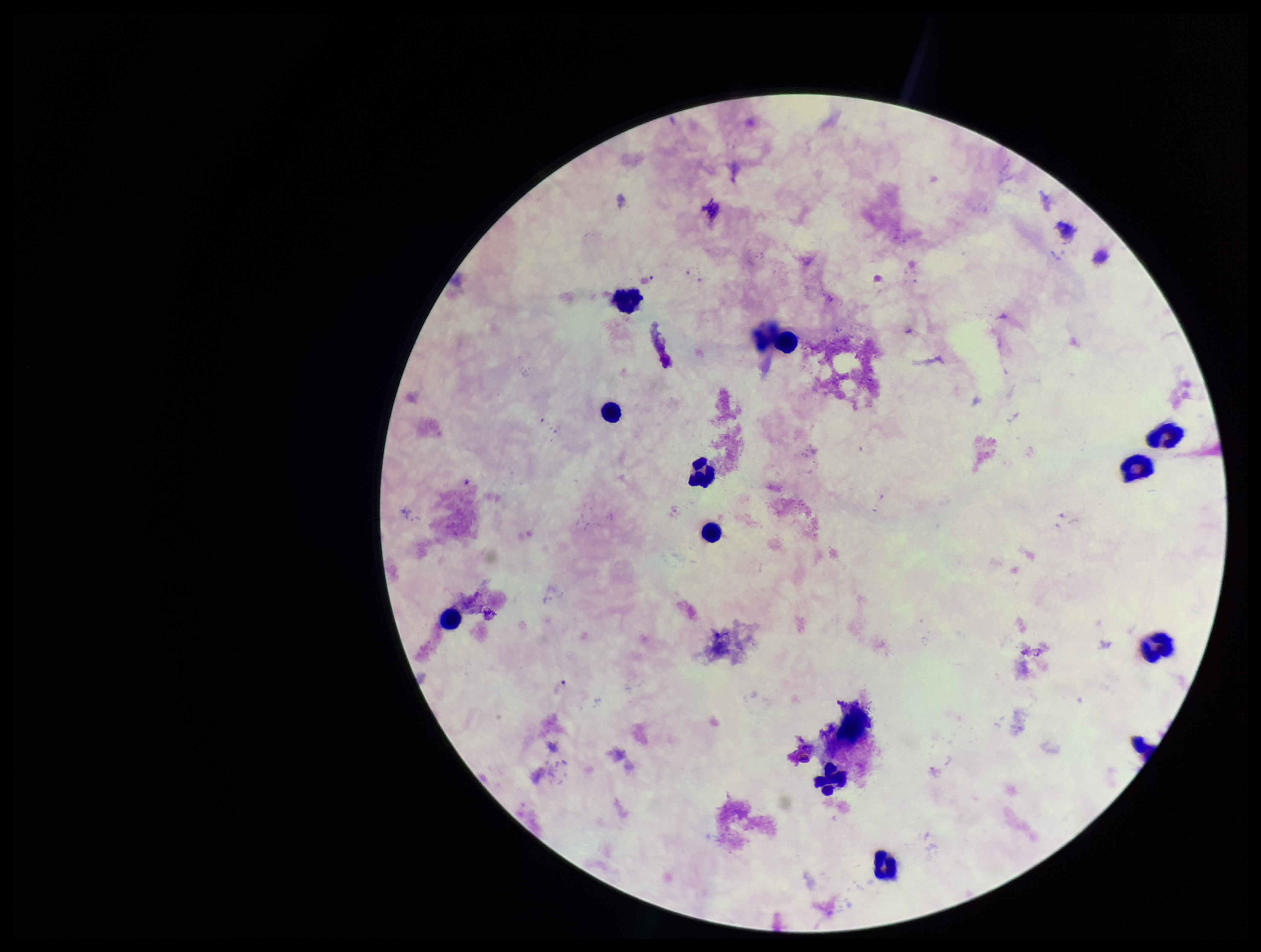
preparation = thick blood smear
Plasmodium parasites = none identified
stain = Giemsa
field of view = single
image size = 1261×952 pixels
patient malaria status = negative
leukocyte count = 12
parasite count = 0
capture = smartphone photograph through the microscope eyepiece